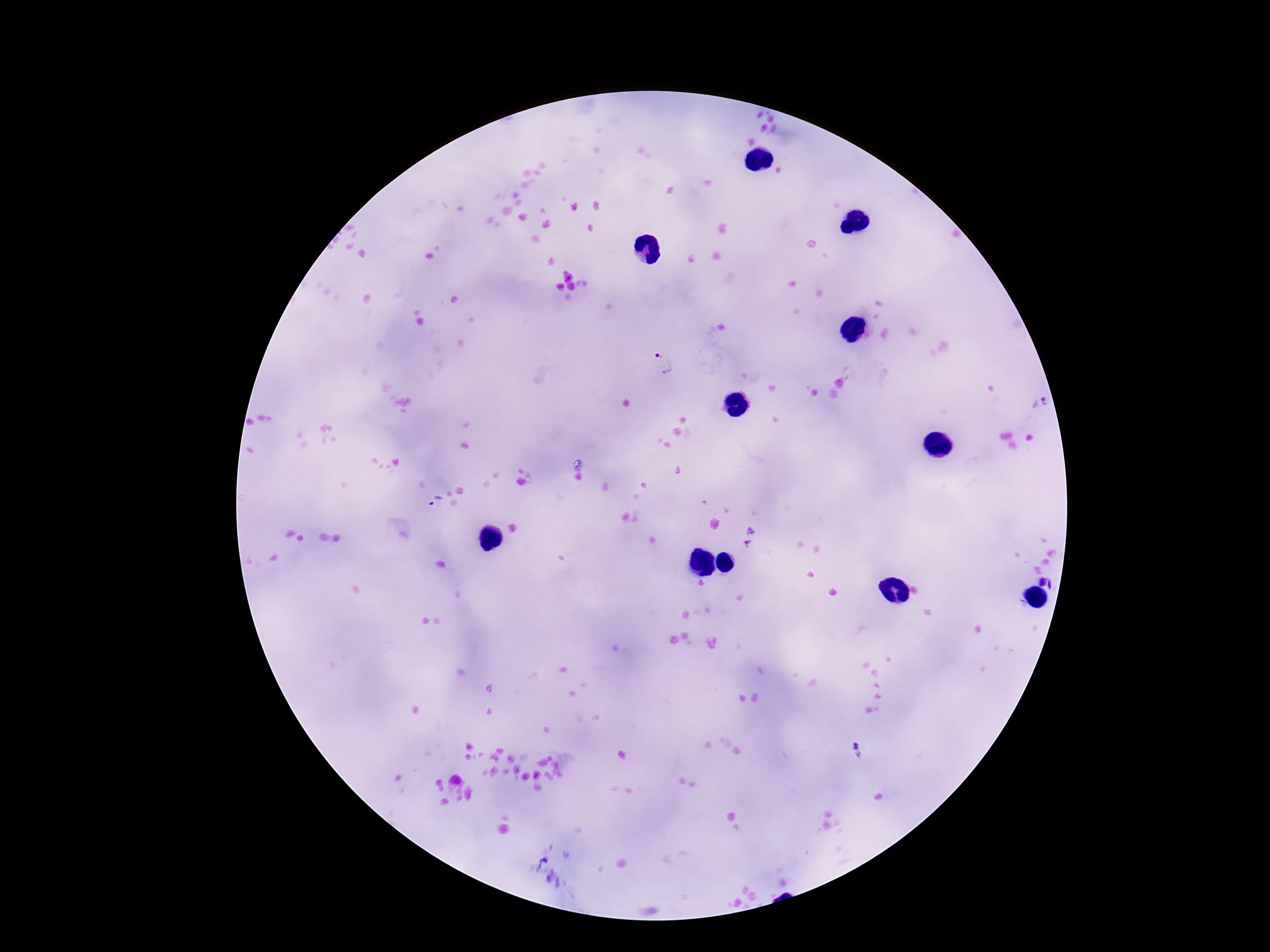 Approximate object centers, in pixels from the top-left corner. Plasmodium parasite locations: (x=663, y=365), (x=435, y=501), (x=750, y=530), (x=748, y=546), (x=1049, y=580), (x=858, y=750). Image is 1270×952 pixels. Single field of view. Smartphone photograph taken through the microscope eyepiece. Thick blood smear. 100x magnification. Giemsa stain. Patient malaria status: infected.